Assess this cell for malaria.
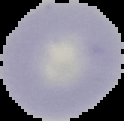

Uninfected.

From a thin blood film. Image is 124×121 pixels. Segmented cell region on a black background.